Report the malaria status of this cell.
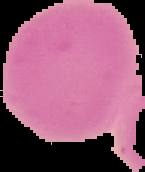

Uninfected.

Summary:
  - Image size: 145×172 pixels
  - Preparation: thin blood smear
  - Image type: cell region segmented out of the field of view; surrounding area masked to black